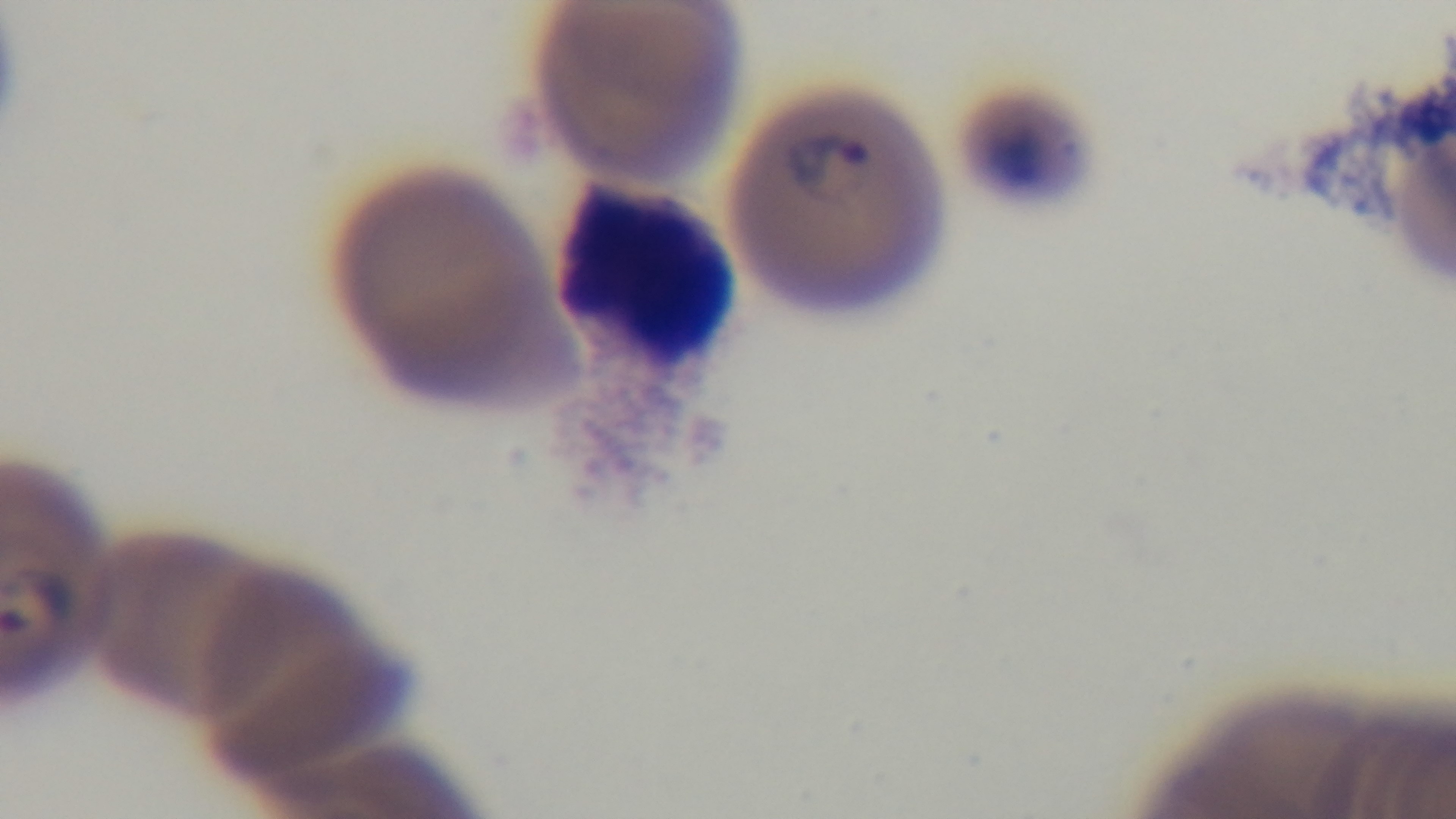

preparation = thin
objective = 100x oil immersion
malaria status = infected
field of view = one from the slide
stain = Giemsa
modality = light microscopy
capture = mounted 4K digital camera